State which cell type is depicted.
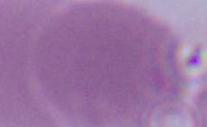
An erythrocyte.

modality = photomicrograph
magnification = 1000x